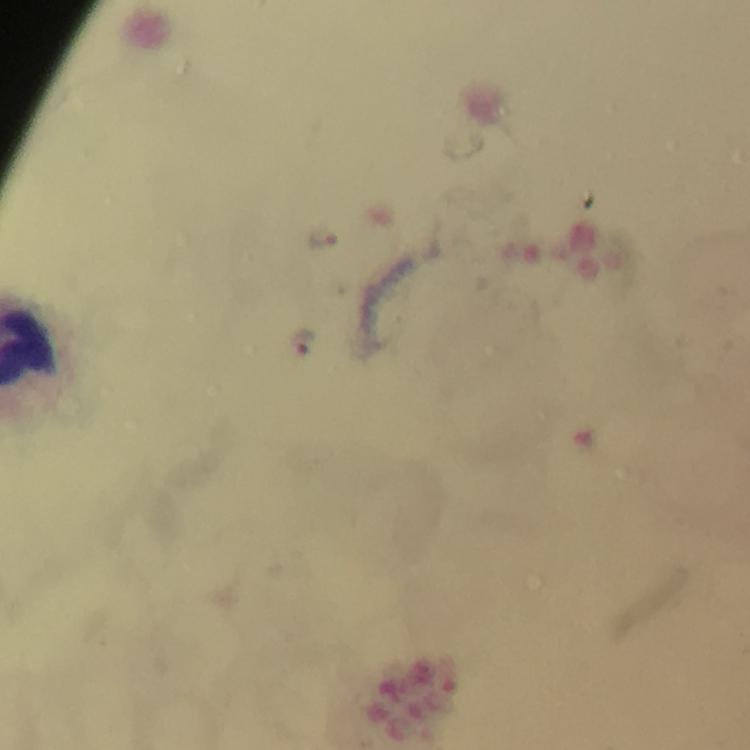
Approximate object centers, in pixels from the top-left corner.
Summary:
  - Plasmodium parasite locations: (x=323, y=238), (x=303, y=341)
  - Cropped from: a single field of view
  - Capture: smartphone mounted on the microscope
  - Image size: 750×750 pixels
  - Stain: Giemsa
  - Preparation: thick blood smear
  - Magnification: 100x
  - Immersion oil: used
  - Context: from a diagnostic examination for malaria